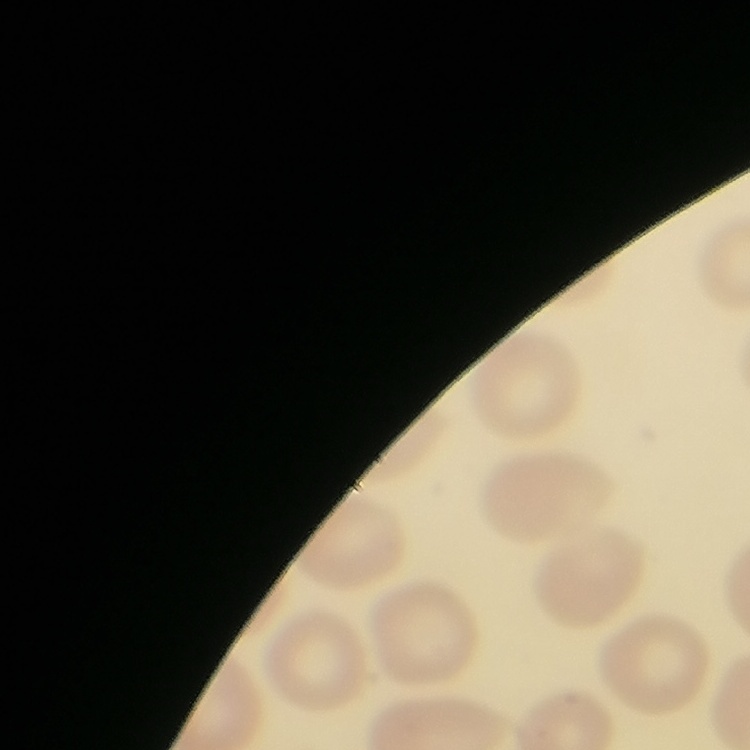
The erythrocytes show no rouleaux formation. Field's or Giemsa stain. Square crop of a larger photomicrograph. Thin blood smear.